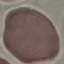 Result: no malaria parasites detected. Giemsa-stained preparation. Acquired by smartphone through the microscope eyepiece. Thin smear of blood. Cell patch, automatically extracted from a larger field of view and resized to 64 × 64 pixels.